Report the malaria status of this cell.
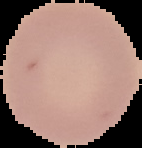

It is uninfected.

Summary:
  - Image type: segmented cell region with the area outside set to black
  - Preparation: thin blood film
  - Image size: 142×148 pixels